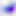

Summary:
  - Magnification: 400x
  - Identification: Toxoplasma gondii
  - Modality: micrograph